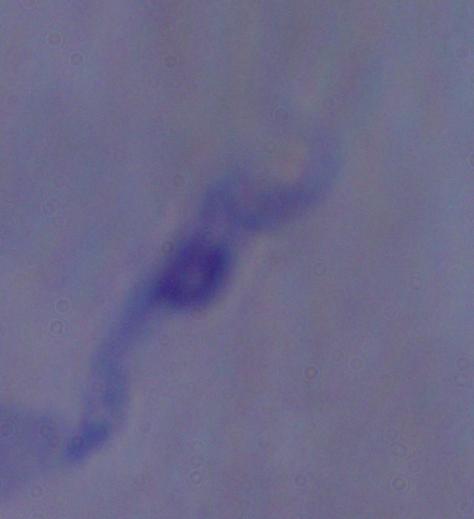 1000x magnification. A trypanosome is seen. Photomicrograph.